Outline each blood parasite and name the species.
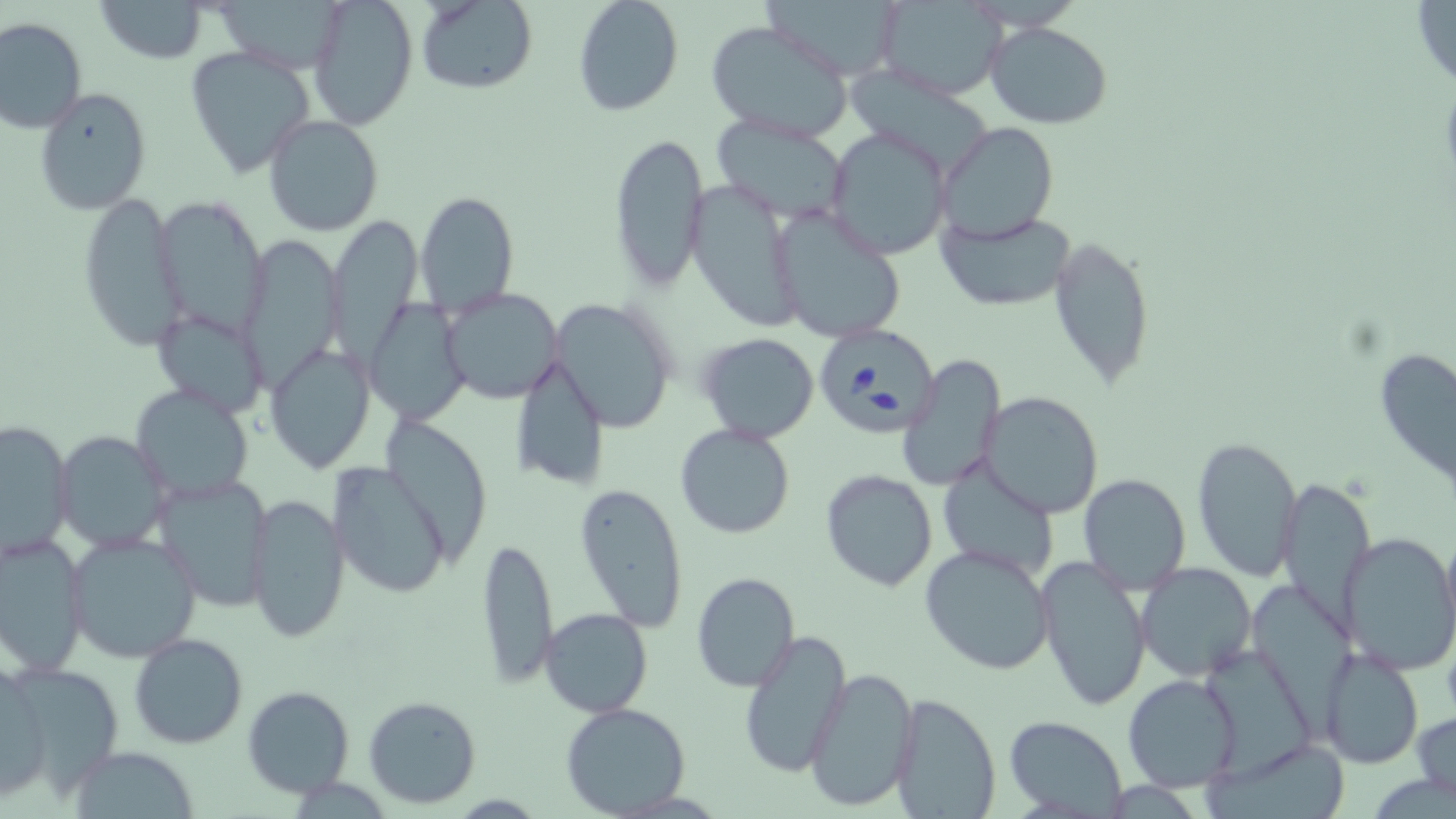
Approximate bounding boxes as (x1, y1, x2, y2) in pixels.
Babesia divergens-infected red blood cells: (813, 321, 940, 435).
No Plasmodium falciparum, Plasmodium ovale, Plasmodium malariae, Plasmodium vivax, or Trypanosoma brucei observed.

Uninfected red blood cell locations: (96, 0, 208, 63), (306, 0, 419, 132), (417, 0, 537, 95), (573, 0, 684, 117), (757, 0, 906, 81), (876, 1, 1007, 98), (1412, 1, 1456, 92), (0, 17, 88, 133), (705, 20, 852, 142), (985, 21, 1112, 129), (184, 46, 316, 179), (852, 69, 997, 178), (35, 86, 152, 216), (262, 114, 385, 238), (709, 114, 853, 223), (939, 122, 1059, 243), (826, 129, 951, 261), (610, 130, 709, 295), (690, 184, 810, 332), (415, 191, 519, 316), (77, 194, 183, 352), (152, 198, 276, 341), (772, 206, 907, 345), (938, 211, 1076, 310), (327, 212, 422, 359), (238, 232, 342, 392), (1048, 236, 1156, 389), (441, 287, 563, 402), (368, 297, 466, 424), (550, 299, 680, 433), (151, 310, 268, 414), (696, 332, 821, 443), (265, 342, 376, 473), (1375, 347, 1456, 484), (899, 354, 1005, 492), (509, 357, 611, 492), (131, 385, 255, 503), (980, 391, 1103, 518), (1, 419, 74, 561), (675, 423, 796, 538), (53, 432, 173, 553), (1191, 436, 1301, 581), (327, 460, 454, 601), (939, 463, 1060, 583), (820, 468, 938, 591), (1078, 472, 1190, 594), (155, 473, 273, 614), (1280, 478, 1372, 648), (266, 481, 423, 624), (574, 483, 688, 633), (247, 492, 351, 645), (1440, 525, 1456, 652), (0, 531, 89, 678), (1338, 531, 1456, 675), (67, 533, 202, 662), (476, 536, 559, 691), (919, 544, 1056, 675), (1037, 556, 1153, 714), (1135, 563, 1257, 683), (691, 572, 800, 692), (1247, 577, 1350, 737), (539, 608, 653, 717), (737, 631, 851, 778), (130, 633, 248, 749), (1198, 646, 1321, 789), (1319, 648, 1423, 768), (0, 661, 48, 803), (8, 661, 126, 801), (804, 666, 919, 813), (1121, 672, 1241, 792), (243, 686, 354, 798), (888, 692, 1003, 818), (363, 695, 482, 808), (560, 703, 693, 817), (1412, 709, 1456, 800), (1005, 714, 1129, 816), (1202, 740, 1353, 819), (70, 745, 200, 818). Slide-level diagnosis: Babesia divergens. Single field of view. May-Grünwald-Giemsa stain. Captured at 1000x magnification. Optical microscopy. Thin blood film. Image is 1456×819 pixels.